Report the malaria status of this cell.
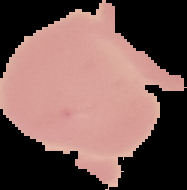
Uninfected.

Image is 187×190 pixels. From a thin blood smear. Segmented cell region on a black background.